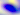

Summary:
  - Identification: Toxoplasma gondii
  - Magnification: 400x
  - Modality: photomicrograph